Assess for parasitized red blood cells.
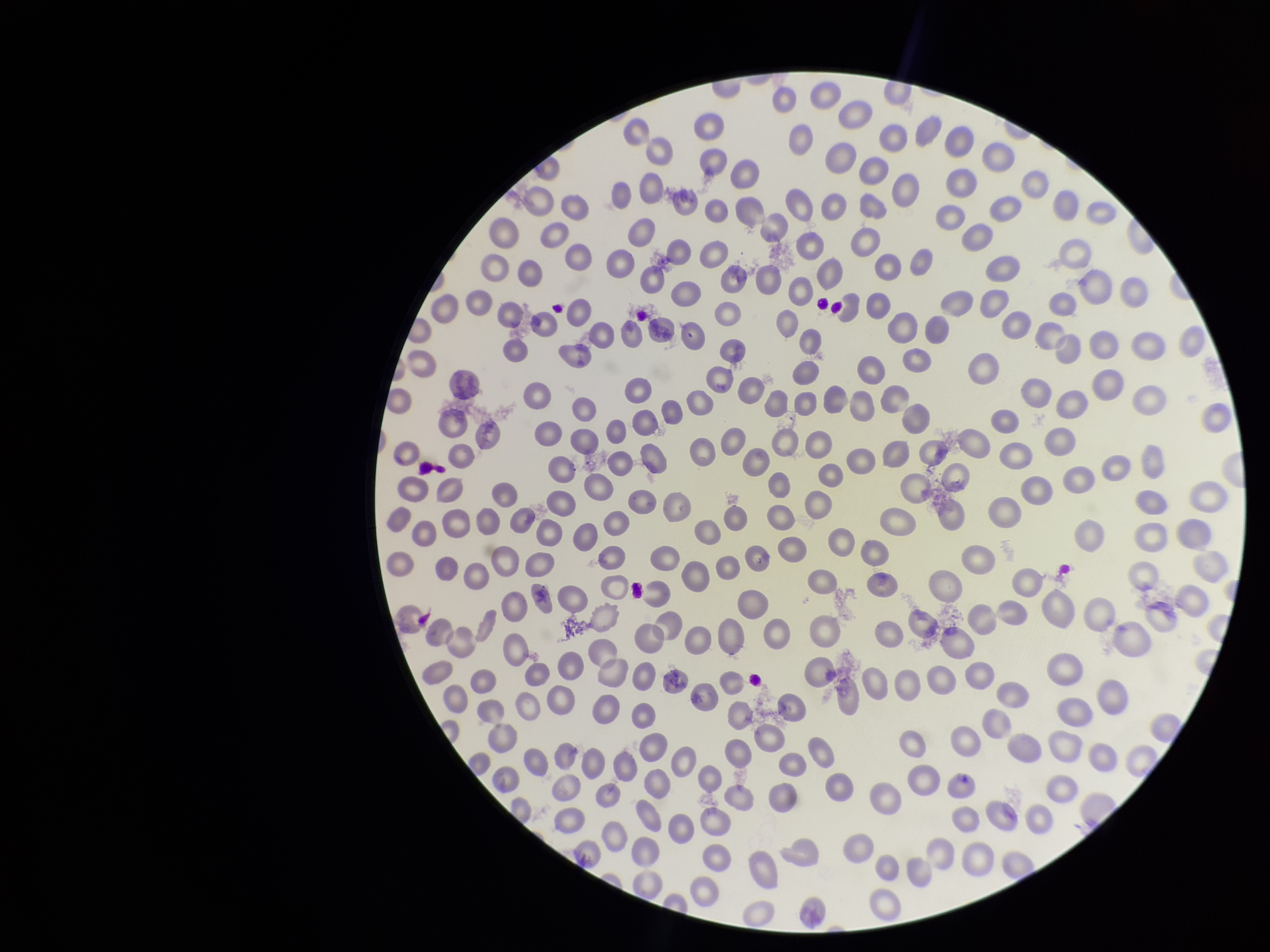

None identified.

{
  "parasitized_red_blood_cell_count": 0,
  "preparation": "thin",
  "patient_malaria_status": "infected",
  "species_reported_for_this_patient": "Plasmodium vivax",
  "red_blood_cell_count": 277,
  "image_size": "1270×952 pixels",
  "capture": "smartphone photograph through the microscope eyepiece",
  "stain": "Giemsa",
  "field_of_view": "single"
}